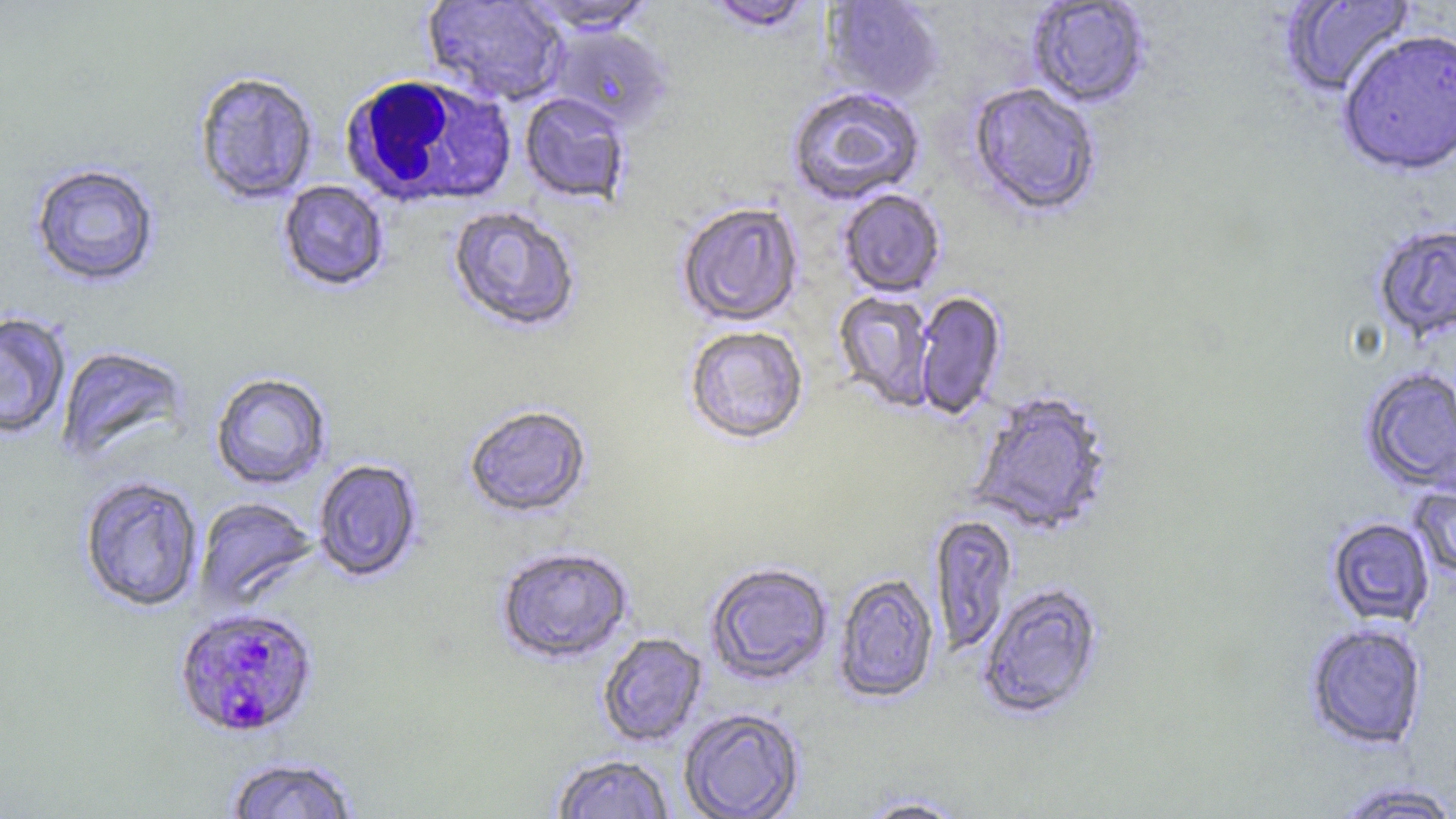

Summary:
  - Coordinate format: approximate bounding boxes as (x1,y1)-(x2,y2) corner pairs in pixels
  - White blood cell locations: (338,74)-(517,209)
  - Plasmodium falciparum-infected red blood cell locations: (172,606)-(320,739)
  - Uninfected red blood cell locations: (1279,0)-(1415,99), (421,1)-(570,106), (522,1)-(657,34), (703,1)-(818,33), (821,1)-(944,103), (1027,1)-(1151,109), (547,24)-(673,129), (1337,31)-(1456,178), (193,70)-(320,205), (967,84)-(1101,219), (786,86)-(925,205), (519,92)-(632,205), (29,162)-(161,287), (277,180)-(390,293), (837,189)-(946,298), (676,202)-(804,327), (447,205)-(581,334), (1372,222)-(1456,344), (833,291)-(937,411), (913,291)-(1007,421), (0,312)-(72,441), (683,325)-(809,446), (55,345)-(190,467), (1359,367)-(1456,495), (210,371)-(332,490), (968,390)-(1115,537), (463,404)-(592,520), (312,458)-(423,583), (78,475)-(205,612), (1408,480)-(1456,583), (194,496)-(319,611), (929,513)-(1018,656), (1326,518)-(1436,627), (495,544)-(635,665), (705,562)-(833,685), (833,573)-(939,704), (976,582)-(1106,721), (1305,623)-(1428,750), (596,632)-(708,747), (678,708)-(805,819), (551,754)-(675,818), (226,755)-(360,818), (1330,781)-(1456,819), (855,794)-(970,818)
  - Slide-level diagnosis: Plasmodium falciparum
  - Stain: May-Grünwald-Giemsa
  - Field of view: one of a larger specimen
  - Modality: optical microscopy
  - Magnification: 1000x
  - Preparation: thin blood smear
  - Image size: 1456×819 pixels